Give the extent of all Plasmodium ovale-infected red blood cells.
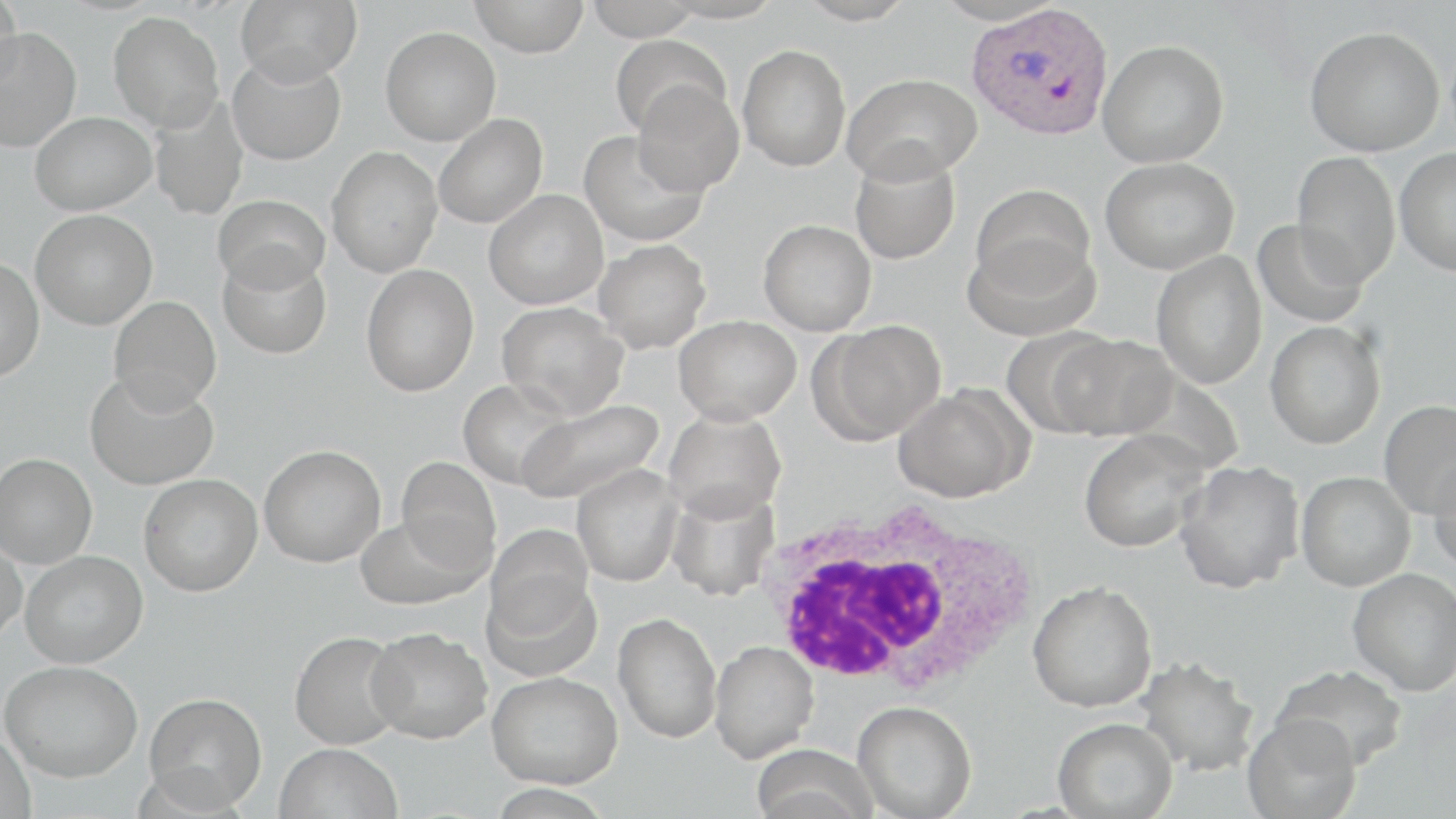
Approximate bounding boxes as [x1, y1, x2, y2] in pixels.
Plasmodium ovale-infected red blood cells: [967, 3, 1114, 141].

slide-level diagnosis = Plasmodium ovale
modality = optical microscopy
preparation = thin blood smear
uninfected red blood cell locations = approximate bounding boxes as [x1, y1, x2, y2] in pixels: [1, 0, 24, 93], [235, 0, 363, 86], [468, 0, 590, 57], [583, 0, 703, 41], [659, 0, 785, 24], [795, 0, 917, 25], [932, 0, 1066, 26], [108, 11, 224, 132], [1, 26, 81, 152], [1304, 26, 1445, 156], [380, 27, 501, 145], [610, 33, 732, 139], [1098, 39, 1229, 168], [737, 44, 851, 172], [227, 53, 346, 166], [843, 73, 982, 184], [632, 81, 744, 196], [148, 95, 248, 221], [30, 111, 156, 215], [434, 113, 548, 228], [578, 128, 709, 247], [326, 146, 443, 277], [1394, 147, 1456, 276], [849, 150, 961, 264], [1291, 152, 1401, 286], [1100, 157, 1238, 275], [971, 184, 1095, 295], [483, 190, 608, 310], [213, 194, 330, 292], [31, 210, 157, 329], [1252, 217, 1370, 329], [758, 219, 876, 336], [963, 234, 1100, 341], [593, 239, 711, 353], [218, 248, 331, 359], [1151, 250, 1267, 389], [0, 256, 45, 381], [361, 264, 479, 396], [108, 296, 221, 414], [496, 302, 629, 418], [673, 315, 801, 425], [811, 320, 946, 445], [1265, 321, 1385, 449], [1000, 329, 1120, 438], [1051, 333, 1178, 441], [84, 370, 218, 490], [457, 378, 577, 490], [893, 384, 1030, 503], [514, 398, 663, 506], [1378, 399, 1456, 519], [663, 408, 786, 522], [1078, 428, 1212, 552], [258, 445, 385, 567], [0, 453, 97, 568], [1428, 454, 1456, 576], [395, 457, 501, 577], [1174, 460, 1304, 593], [572, 465, 684, 586], [1295, 471, 1416, 591], [138, 474, 262, 596], [666, 484, 781, 601], [355, 514, 482, 610], [485, 524, 593, 639], [0, 537, 26, 647], [21, 550, 148, 667], [481, 567, 602, 682], [1347, 568, 1456, 696], [1027, 580, 1158, 713], [613, 613, 722, 743], [366, 627, 493, 744], [289, 631, 408, 749], [709, 640, 818, 762], [1135, 656, 1261, 776], [1, 660, 142, 782], [1271, 664, 1409, 770], [487, 671, 622, 788], [144, 692, 267, 812], [853, 700, 976, 819], [1242, 714, 1362, 819], [1052, 717, 1178, 818], [0, 728, 35, 819], [274, 743, 402, 819], [749, 744, 877, 819], [483, 784, 616, 819]
magnification = 1000x
stain = May-Grünwald-Giemsa
white blood cell locations = approximate bounding boxes as [x1, y1, x2, y2] in pixels: [756, 493, 1040, 700]
field of view = one of a larger specimen
image size = 1456×819 pixels